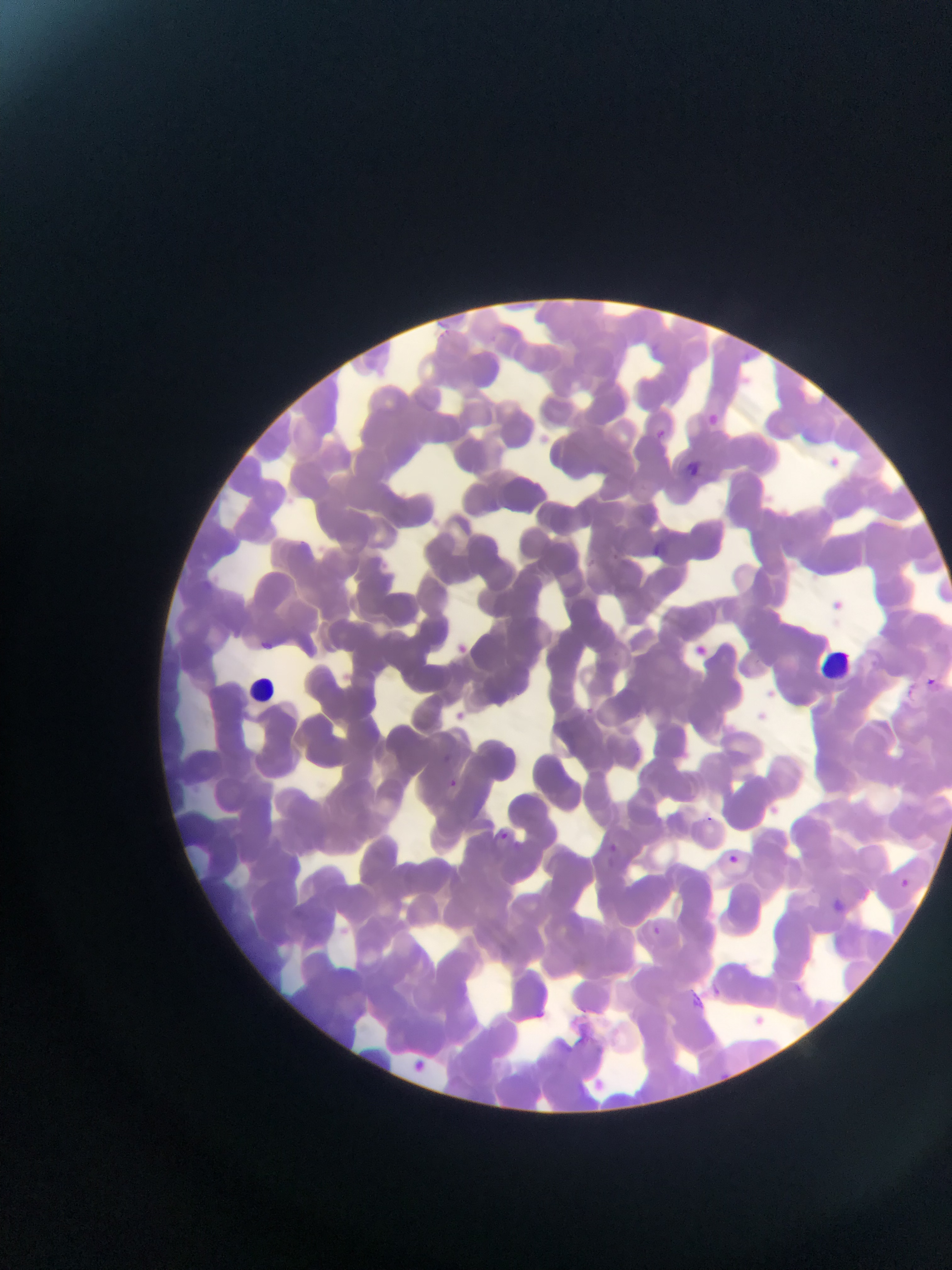
Approximate bounding boxes as {left, top, right, bottom} in pixels.
Summary:
  - Leukocyte locations: {826, 647, 856, 678}, {245, 673, 281, 708}
  - Malaria parasite locations: {745, 352, 755, 361}, {707, 412, 719, 425}, {656, 424, 669, 435}, {655, 428, 666, 440}, {686, 461, 702, 476}, {651, 541, 666, 555}, {259, 639, 275, 652}, {927, 676, 937, 686}, {585, 704, 596, 715}, {442, 752, 451, 763}, {448, 777, 458, 788}, {500, 830, 510, 839}, {608, 841, 619, 853}, {728, 853, 739, 864}, {900, 877, 909, 886}, {831, 897, 846, 912}, {652, 924, 662, 934}, {792, 983, 803, 994}, {708, 984, 722, 999}, {688, 990, 706, 1009}
  - Image size: 952×1270 pixels
  - Preparation: thin blood film
  - Country: Ghana
  - Capture: mobile-phone photograph through a microscope
  - Field of view: single